Locate every blood parasite and identify its species.
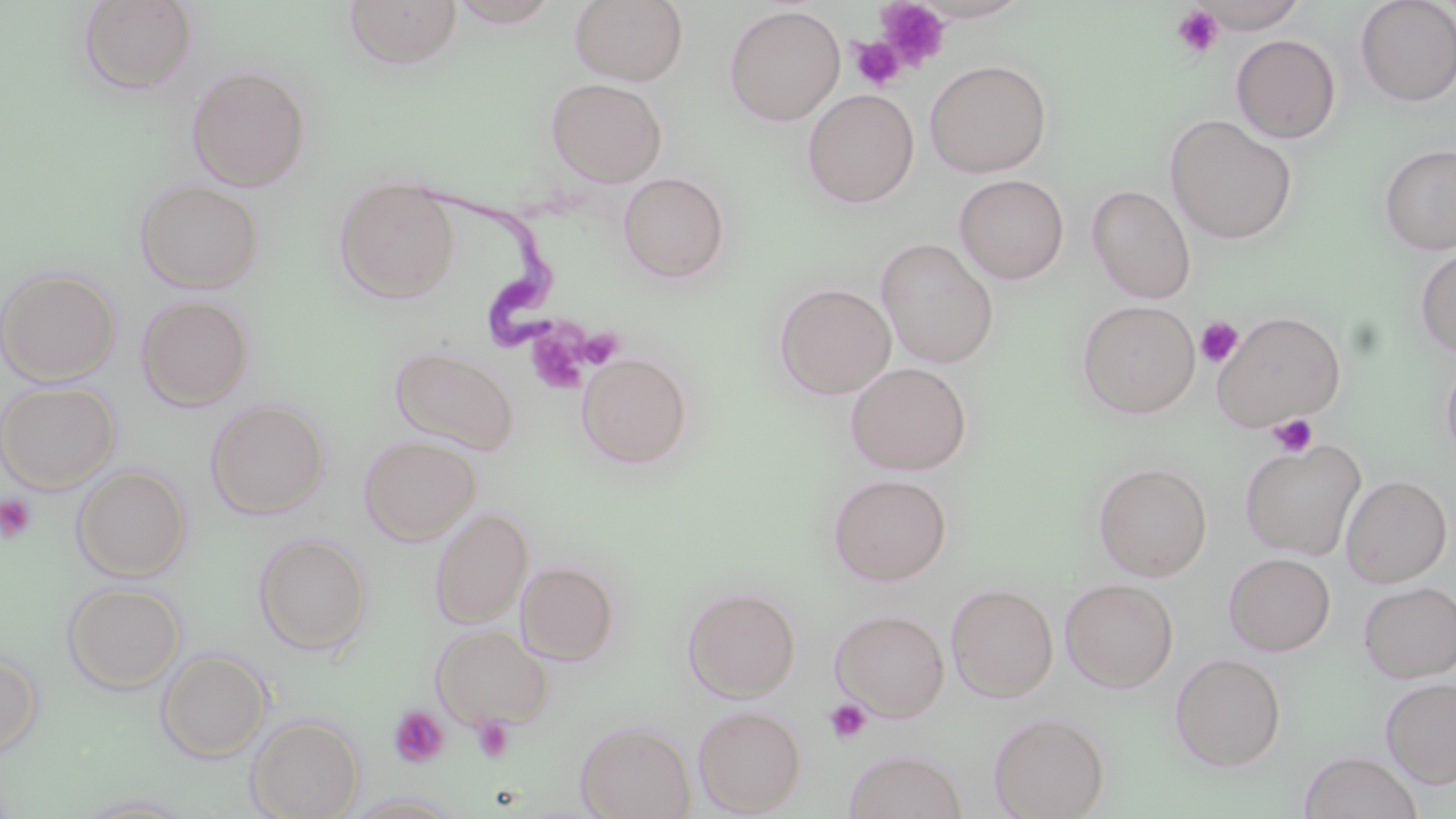
Approximate bounding boxes as named x1/y1/x2/y2 corners in pixels.
Trypanosoma brucei: (x1=421, y1=185, x2=571, y2=348).
No Plasmodium falciparum, Plasmodium ovale, Plasmodium malariae, Plasmodium vivax, or Babesia divergens observed.

Summary:
  - Uninfected red blood cell locations: (x1=569, y1=0, x2=689, y2=85), (x1=1191, y1=0, x2=1311, y2=34), (x1=1355, y1=0, x2=1456, y2=106), (x1=77, y1=1, x2=199, y2=95), (x1=343, y1=1, x2=463, y2=70), (x1=447, y1=1, x2=562, y2=27), (x1=724, y1=5, x2=845, y2=125), (x1=1231, y1=34, x2=1342, y2=144), (x1=924, y1=59, x2=1052, y2=178), (x1=186, y1=65, x2=311, y2=191), (x1=546, y1=77, x2=667, y2=187), (x1=803, y1=89, x2=919, y2=208), (x1=1164, y1=115, x2=1298, y2=244), (x1=1378, y1=142, x2=1456, y2=255), (x1=618, y1=172, x2=730, y2=284), (x1=954, y1=174, x2=1069, y2=284), (x1=334, y1=176, x2=461, y2=303), (x1=134, y1=179, x2=264, y2=293), (x1=1087, y1=184, x2=1196, y2=303), (x1=876, y1=238, x2=999, y2=368), (x1=1414, y1=245, x2=1456, y2=358), (x1=0, y1=267, x2=122, y2=385), (x1=774, y1=282, x2=896, y2=399), (x1=136, y1=294, x2=253, y2=410), (x1=1077, y1=300, x2=1201, y2=418), (x1=1212, y1=310, x2=1346, y2=430), (x1=389, y1=345, x2=520, y2=454), (x1=1439, y1=349, x2=1456, y2=466), (x1=577, y1=353, x2=693, y2=469), (x1=845, y1=362, x2=972, y2=475), (x1=0, y1=381, x2=120, y2=493), (x1=205, y1=399, x2=330, y2=519), (x1=359, y1=436, x2=480, y2=545), (x1=1239, y1=438, x2=1367, y2=559), (x1=1092, y1=461, x2=1213, y2=580), (x1=72, y1=465, x2=192, y2=581), (x1=827, y1=473, x2=952, y2=586), (x1=1341, y1=475, x2=1452, y2=587), (x1=430, y1=507, x2=533, y2=628), (x1=253, y1=533, x2=372, y2=655), (x1=1224, y1=552, x2=1335, y2=656), (x1=517, y1=561, x2=620, y2=665), (x1=1060, y1=578, x2=1179, y2=692), (x1=1359, y1=581, x2=1456, y2=683), (x1=62, y1=582, x2=185, y2=694), (x1=946, y1=583, x2=1059, y2=701), (x1=683, y1=586, x2=801, y2=701), (x1=830, y1=609, x2=950, y2=720), (x1=432, y1=624, x2=552, y2=729), (x1=156, y1=649, x2=271, y2=763), (x1=0, y1=650, x2=43, y2=759), (x1=1170, y1=653, x2=1287, y2=772), (x1=1382, y1=677, x2=1456, y2=788), (x1=693, y1=705, x2=807, y2=815), (x1=988, y1=711, x2=1110, y2=819), (x1=246, y1=715, x2=364, y2=819), (x1=575, y1=721, x2=696, y2=819), (x1=843, y1=749, x2=968, y2=819), (x1=1299, y1=752, x2=1423, y2=819), (x1=342, y1=792, x2=467, y2=818), (x1=71, y1=793, x2=201, y2=817)
  - Platelet locations: (x1=876, y1=1, x2=952, y2=71), (x1=1171, y1=4, x2=1224, y2=58), (x1=850, y1=37, x2=904, y2=91), (x1=1195, y1=316, x2=1243, y2=367), (x1=524, y1=328, x2=589, y2=396), (x1=576, y1=328, x2=625, y2=369), (x1=1268, y1=413, x2=1319, y2=457), (x1=0, y1=494, x2=37, y2=544), (x1=823, y1=698, x2=872, y2=745), (x1=389, y1=706, x2=450, y2=768), (x1=472, y1=716, x2=515, y2=764)
  - Slide-level diagnosis: Trypanosoma brucei
  - Image size: 1456×819 pixels
  - Preparation: thin blood smear
  - Modality: optical microscopy
  - Stain: May-Grünwald-Giemsa
  - Field of view: single
  - Magnification: 1000x